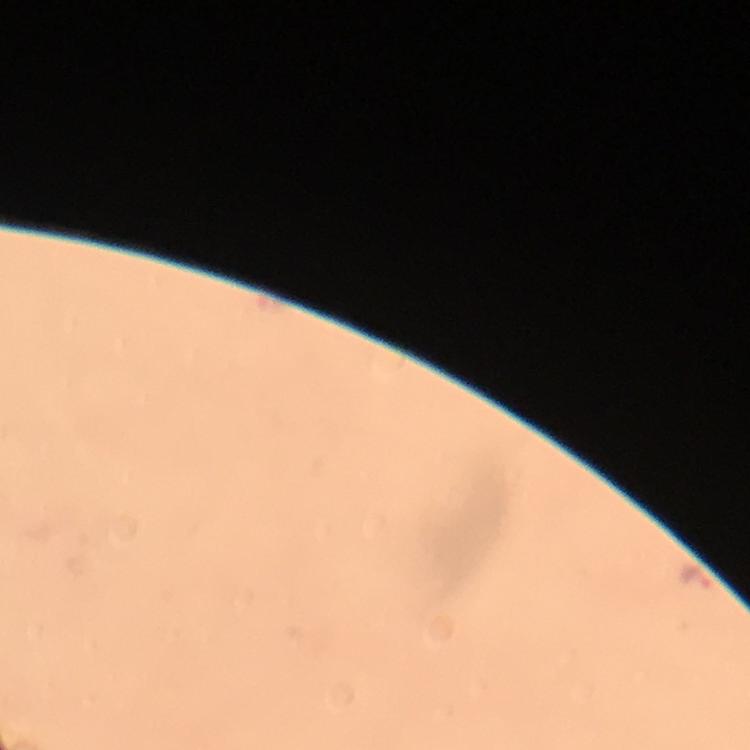

capture = smartphone mounted on the microscope
stain = Giemsa
image size = 750×750 pixels
Plasmodium parasite locations = approximate centers as (x, y) in pixels: (699, 580)
preparation = thick blood film
immersion oil = used
magnification = 100x
cropped from = a single field of view
context = from a diagnostic examination for malaria